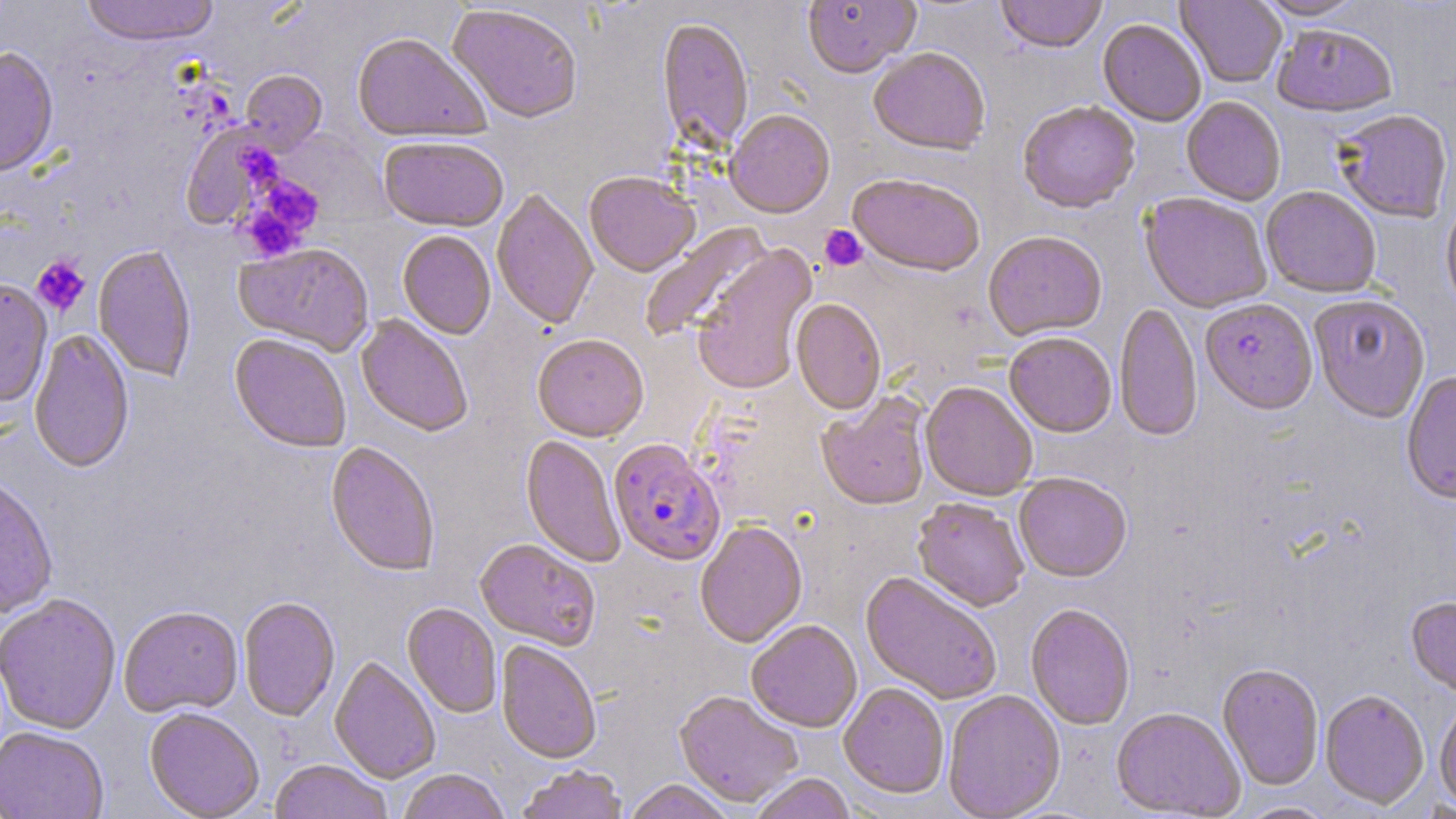
slide_level_diagnosis: Plasmodium falciparum
stain: May-Grünwald-Giemsa
modality: light microscopy
image_size: 1456×819 pixels
preparation: thin blood film
field_of_view: single
plasmodium_falciparum_infected_red_blood_cell_locations: 'approximate bounding boxes as (x1,y1)-(x2,y2) corner pairs in pixels: (1201,301)-(1317,418), (608,441)-(725,568)'
magnification: 1000x
uninfected_red_blood_cell_locations: 'approximate bounding boxes as (x1,y1)-(x2,y2) corner pairs in pixels: (79,0)-(220,49), (802,0)-(921,82), (995,0)-(1108,56), (1175,0)-(1287,89), (1253,0)-(1369,22), (446,6)-(582,127), (657,20)-(753,156), (1098,21)-(1206,128), (1272,27)-(1397,121), (352,36)-(489,146), (0,48)-(59,180), (869,50)-(990,158), (240,71)-(328,155), (1181,98)-(1285,207), (1018,103)-(1140,216), (1334,111)-(1453,225), (724,113)-(835,220), (180,123)-(283,227), (378,140)-(508,235), (584,174)-(700,279), (847,176)-(984,280), (1261,188)-(1381,299), (492,190)-(598,332), (1139,194)-(1271,314), (1441,205)-(1456,318), (640,222)-(775,343), (398,233)-(495,341), (983,233)-(1107,342), (234,244)-(375,358), (691,245)-(820,397), (93,246)-(196,383), (0,280)-(53,409), (1309,297)-(1430,426), (790,299)-(886,417), (1114,303)-(1202,445), (355,316)-(472,438), (29,329)-(134,475), (1004,335)-(1116,440), (229,336)-(351,455), (532,336)-(649,444), (1402,372)-(1456,509), (920,384)-(1037,502), (816,393)-(932,513), (520,436)-(625,568), (325,443)-(440,579), (1014,475)-(1132,585), (0,479)-(59,619), (912,499)-(1029,614), (695,523)-(808,649), (474,540)-(600,651), (860,573)-(1002,706), (0,596)-(121,736), (238,598)-(340,722), (1405,598)-(1456,701), (402,604)-(501,719), (1025,605)-(1135,731), (119,607)-(243,719), (746,621)-(862,734), (496,641)-(601,765), (329,657)-(441,783), (1217,665)-(1324,791), (839,684)-(949,800), (1320,690)-(1429,811), (673,691)-(803,809), (943,691)-(1066,819), (1434,701)-(1456,812), (144,709)-(264,819), (1111,709)-(1245,818), (0,728)-(109,819), (268,761)-(393,819), (514,766)-(630,819), (398,770)-(510,819), (749,774)-(856,819), (622,780)-(735,819), (1235,801)-(1337,819)'
platelet_locations: 'approximate bounding boxes as (x1,y1)-(x2,y2) corner pairs in pixels: (236,151)-(276,188), (238,176)-(323,262), (820,225)-(868,271), (31,255)-(91,316)'